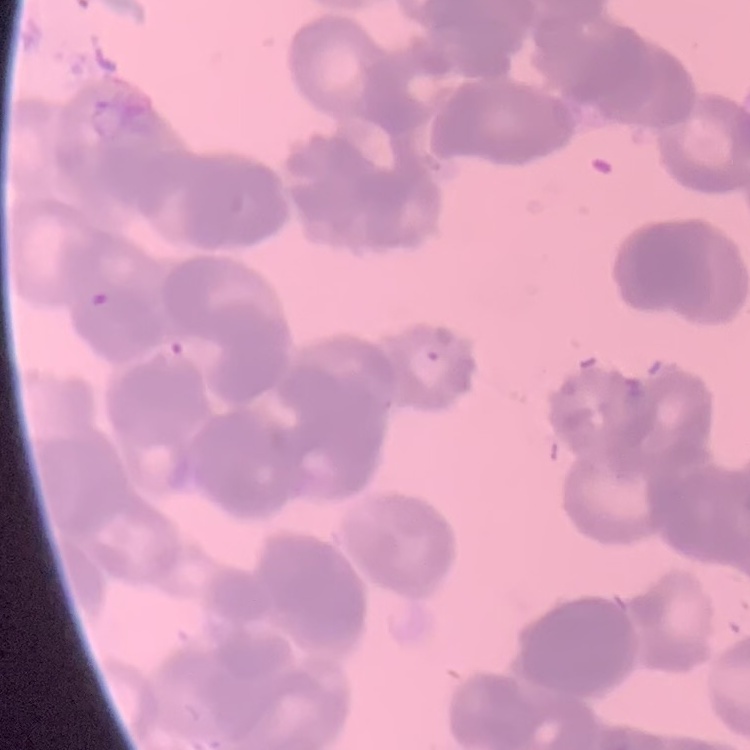

red blood cell morphology = rouleaux formation
stain = Field's or Giemsa
image type = one tile cut from a larger photomicrograph
preparation = thin peripheral smear